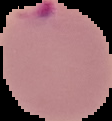

result = malaria parasites identified
preparation = thin blood film
image size = 112×121 pixels
image type = cell region segmented out of the field of view; surrounding area masked to black